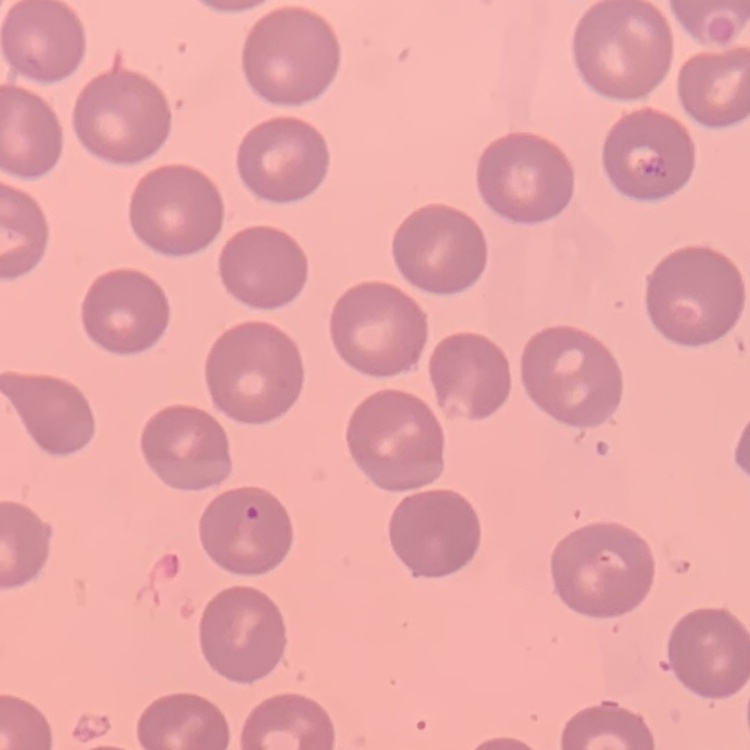
Summary:
  - Red blood cell morphology: no rouleaux formation
  - Image type: one tile cut from a larger photomicrograph
  - Stain: Field's or Giemsa
  - Preparation: thin blood smear